State the preparation type.
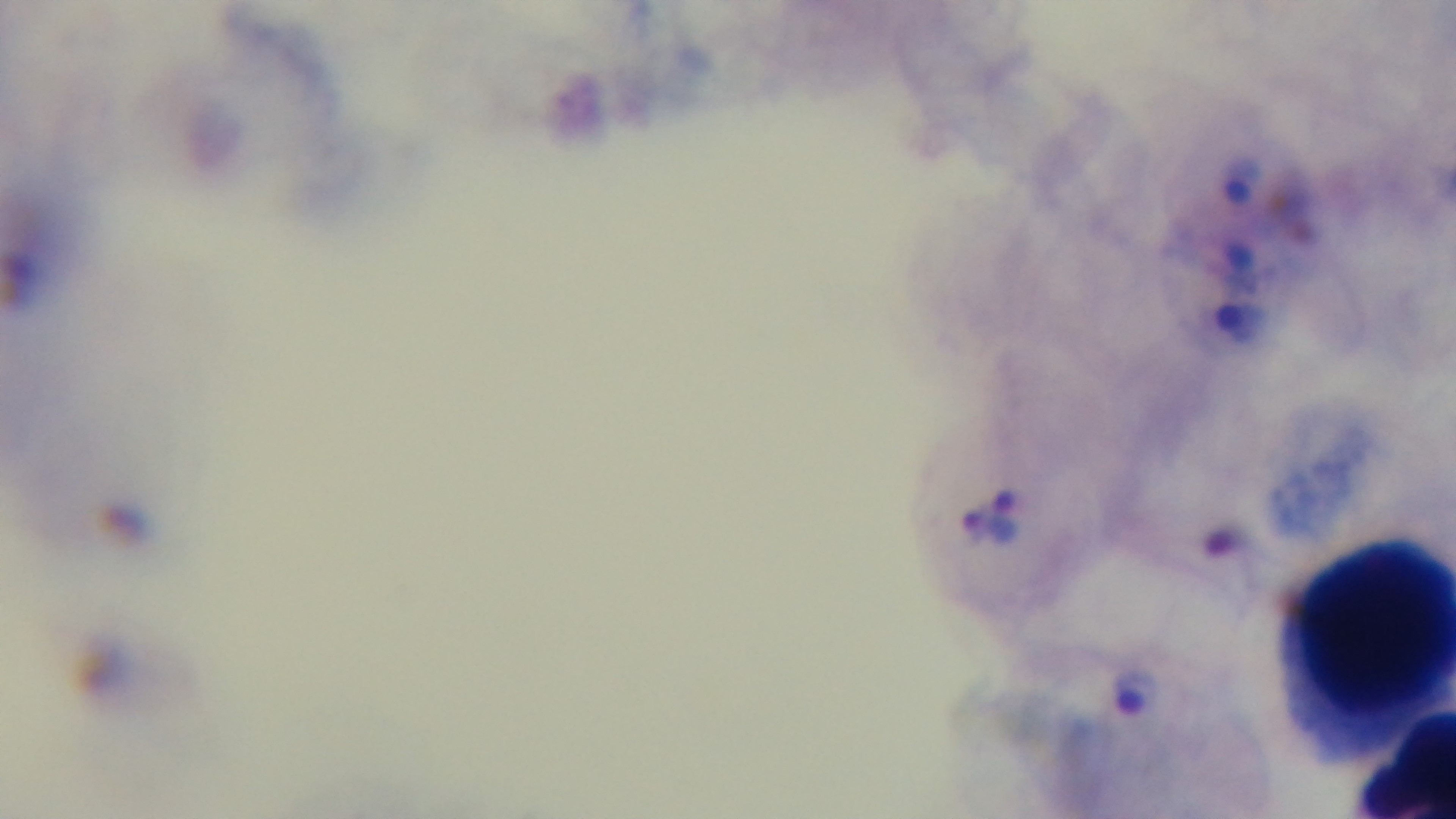

It is a thick blood film.

malaria status = positive
objective = 100x oil immersion
modality = light microscopy
capture = mounted 4K digital camera
stain = Giemsa
field of view = single